Comment on the morphology of the erythrocytes.
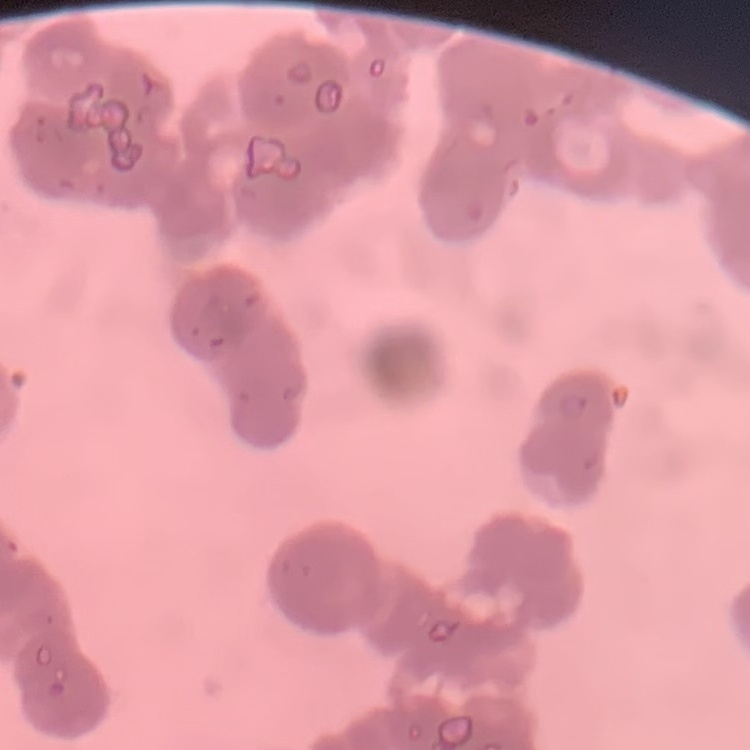
They show rouleaux formation.

preparation = thin blood smear
stain = Field's or Giemsa
image type = one tile cut from a larger photomicrograph